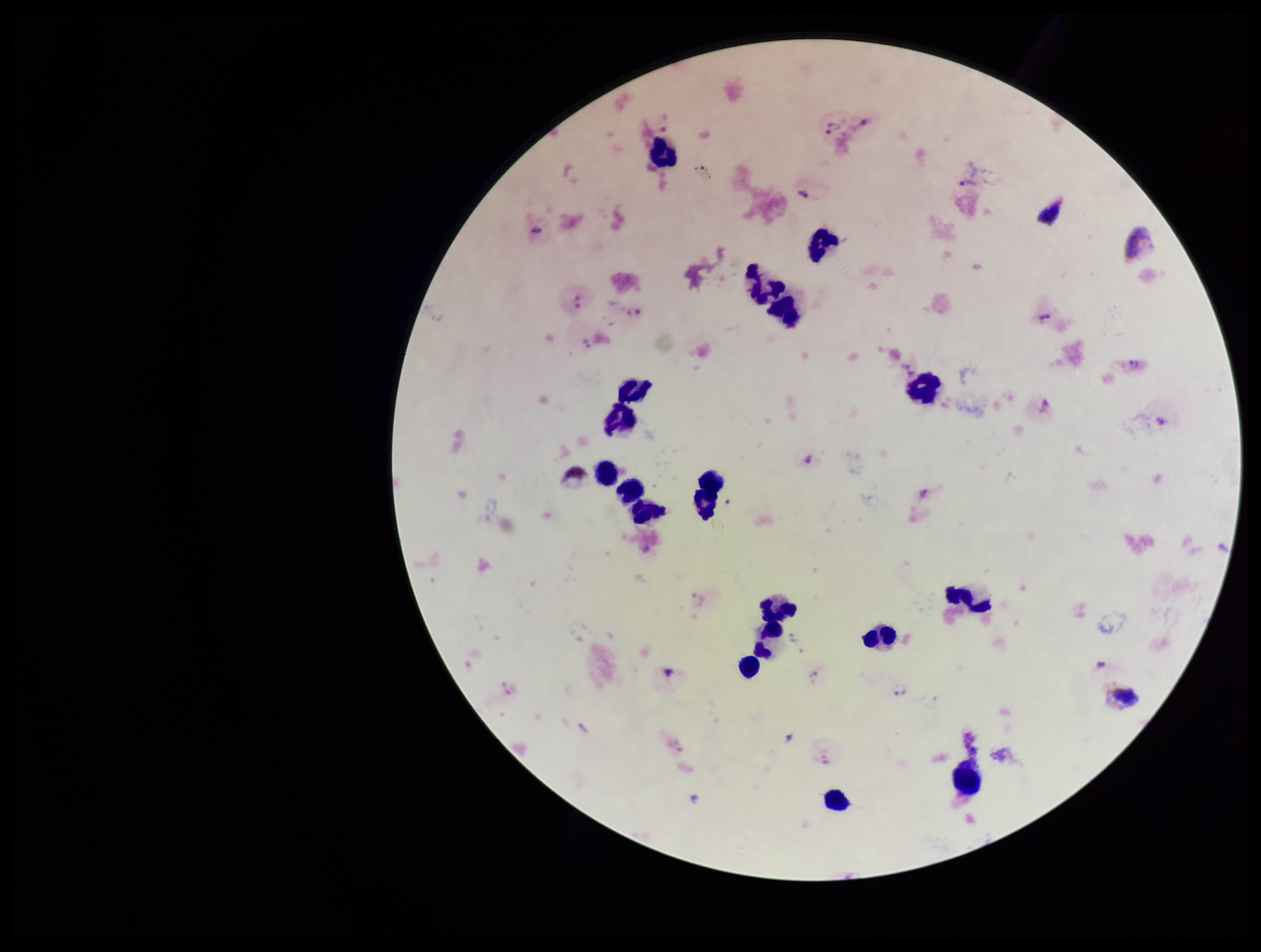

Summary:
  - Plasmodium parasites: seen
  - Stain: Giemsa
  - Species reported for this patient: Plasmodium vivax
  - Image size: 1261×952 pixels
  - Patient malaria status: positive
  - Preparation: thick blood smear
  - Field of view: single
  - Parasite count: 19
  - Capture: smartphone photograph through the microscope eyepiece
  - Leukocyte count: 19